Assess this cell for malaria.
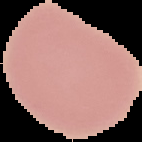

It is uninfected.

From a thin blood smear. Image is 142×142 pixels. Segmented cell region on a black background.